Assess for Plasmodium parasites.
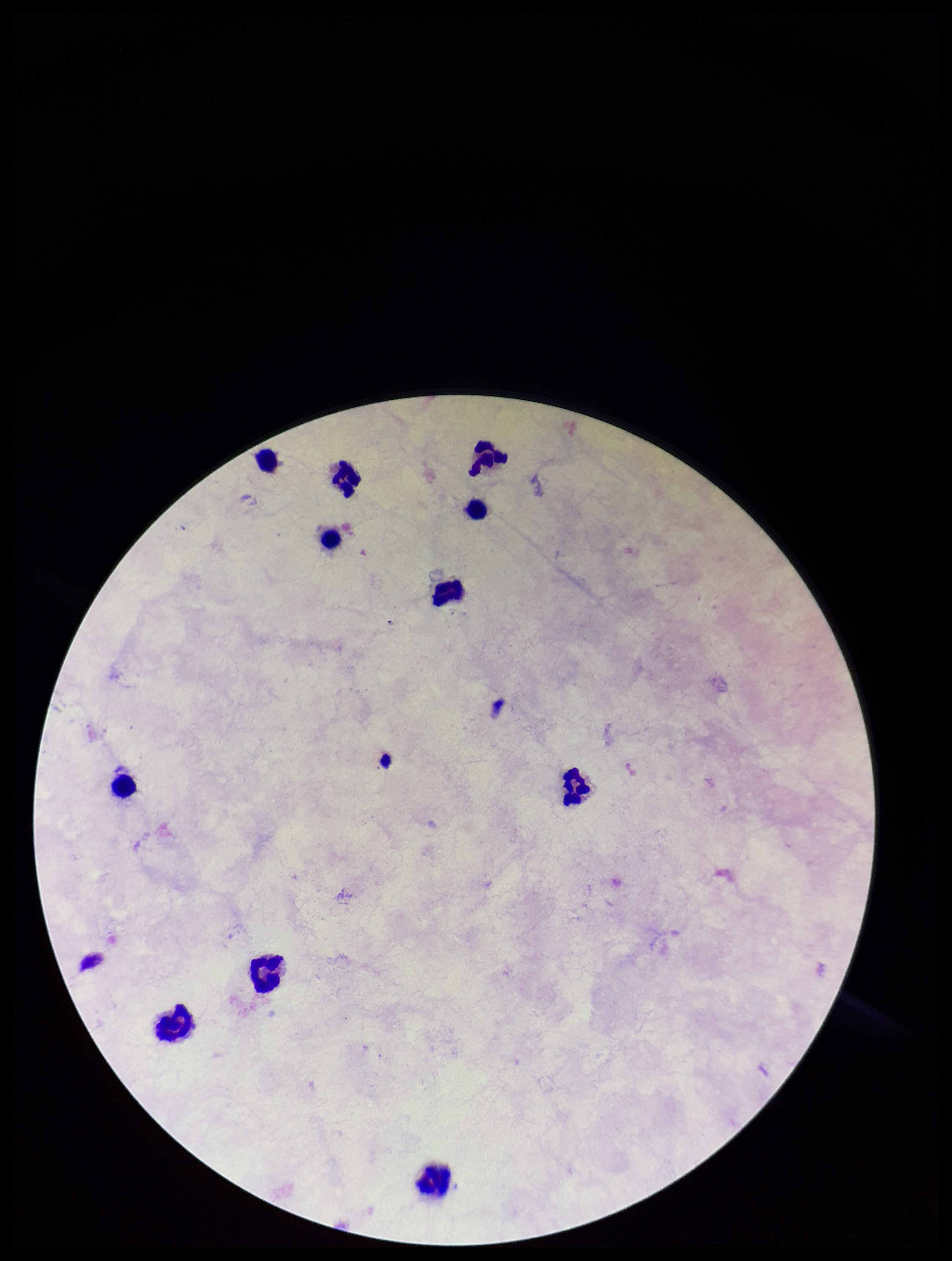

None detected.

stain = Giemsa
parasite count = 0
preparation = thick blood smear
patient malaria status = negative
leukocyte count = 11
image size = 952×1261 pixels
field of view = single
capture = smartphone photograph through the microscope eyepiece